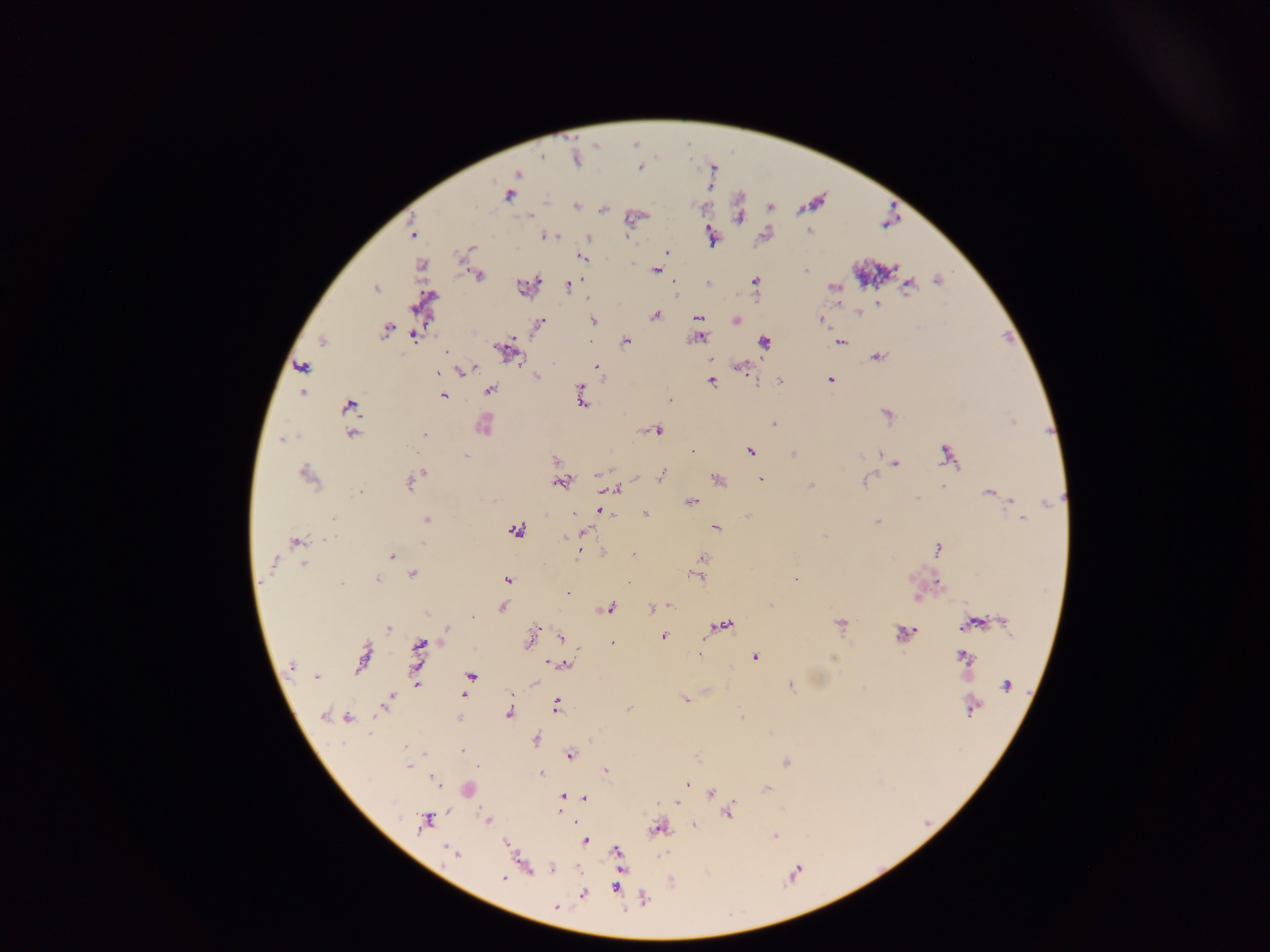
field of view = single
capture = mobile-phone photograph through a microscope
preparation = thick blood smear
image size = 1270×952 pixels
malaria parasite locations = approximate centers as (x, y) in pixels: (639, 170), (518, 175), (509, 196), (529, 216), (738, 218), (590, 238), (472, 248), (668, 251), (580, 257), (461, 263), (656, 269), (804, 273), (478, 276), (539, 279), (754, 281), (938, 281), (575, 283), (566, 284), (909, 284), (376, 290), (877, 304), (413, 307), (655, 314), (697, 319), (818, 319), (594, 320), (736, 321), (540, 322), (384, 331), (414, 337), (515, 337), (700, 339), (323, 341), (626, 342), (765, 343), (842, 343), (496, 346), (446, 351), (448, 352), (876, 357), (519, 359), (710, 360), (598, 367), (300, 368), (740, 368), (461, 373), (536, 377), (754, 377), (830, 379), (780, 380), (711, 382), (491, 391), (581, 391), (303, 392), (443, 395), (581, 399), (670, 399), (349, 404), (886, 414), (773, 425), (659, 431), (424, 433), (352, 434), (283, 440), (943, 449), (693, 451), (752, 452), (880, 453), (793, 454), (944, 454), (860, 455), (465, 456), (554, 460), (897, 464), (599, 473), (306, 474), (421, 474), (662, 476), (867, 478), (716, 479), (761, 479), (862, 481), (558, 482), (410, 484), (811, 485), (942, 487), (613, 489), (988, 492), (916, 497), (1010, 499), (691, 502), (597, 511), (575, 512), (646, 514), (333, 519), (426, 519), (1021, 519), (877, 520), (716, 528), (515, 530), (585, 531), (824, 535), (294, 540), (422, 542), (939, 549), (579, 552), (632, 555), (392, 557), (703, 558), (274, 564), (304, 565), (412, 574), (376, 578), (699, 578), (507, 579), (797, 580), (259, 582), (342, 582), (629, 582), (941, 585), (568, 593), (918, 598), (670, 605), (771, 606), (502, 607), (611, 607), (650, 608), (471, 616), (976, 622), (1004, 623), (840, 625), (727, 626), (446, 627), (964, 627), (537, 628), (388, 630), (901, 633), (531, 637), (662, 637), (559, 638), (702, 640), (613, 643), (420, 646), (700, 654), (960, 654), (967, 656), (755, 657), (552, 663), (564, 664), (290, 668), (360, 668), (318, 676), (469, 677), (535, 682), (417, 683), (790, 686), (1006, 686), (463, 694), (509, 696), (686, 700), (556, 704), (383, 709), (629, 709), (324, 714), (508, 715), (742, 716), (347, 719), (536, 741), (463, 750), (570, 755), (786, 762), (409, 766), (479, 766), (607, 770), (542, 773), (434, 779), (687, 784), (766, 789), (710, 793), (562, 796), (584, 797), (677, 804), (557, 812), (727, 814), (425, 820), (488, 820), (575, 821), (694, 827), (652, 830), (774, 836), (584, 841), (622, 868), (551, 869), (500, 879), (615, 888), (583, 894), (557, 907)
country = Ghana